Identify the preparation type.
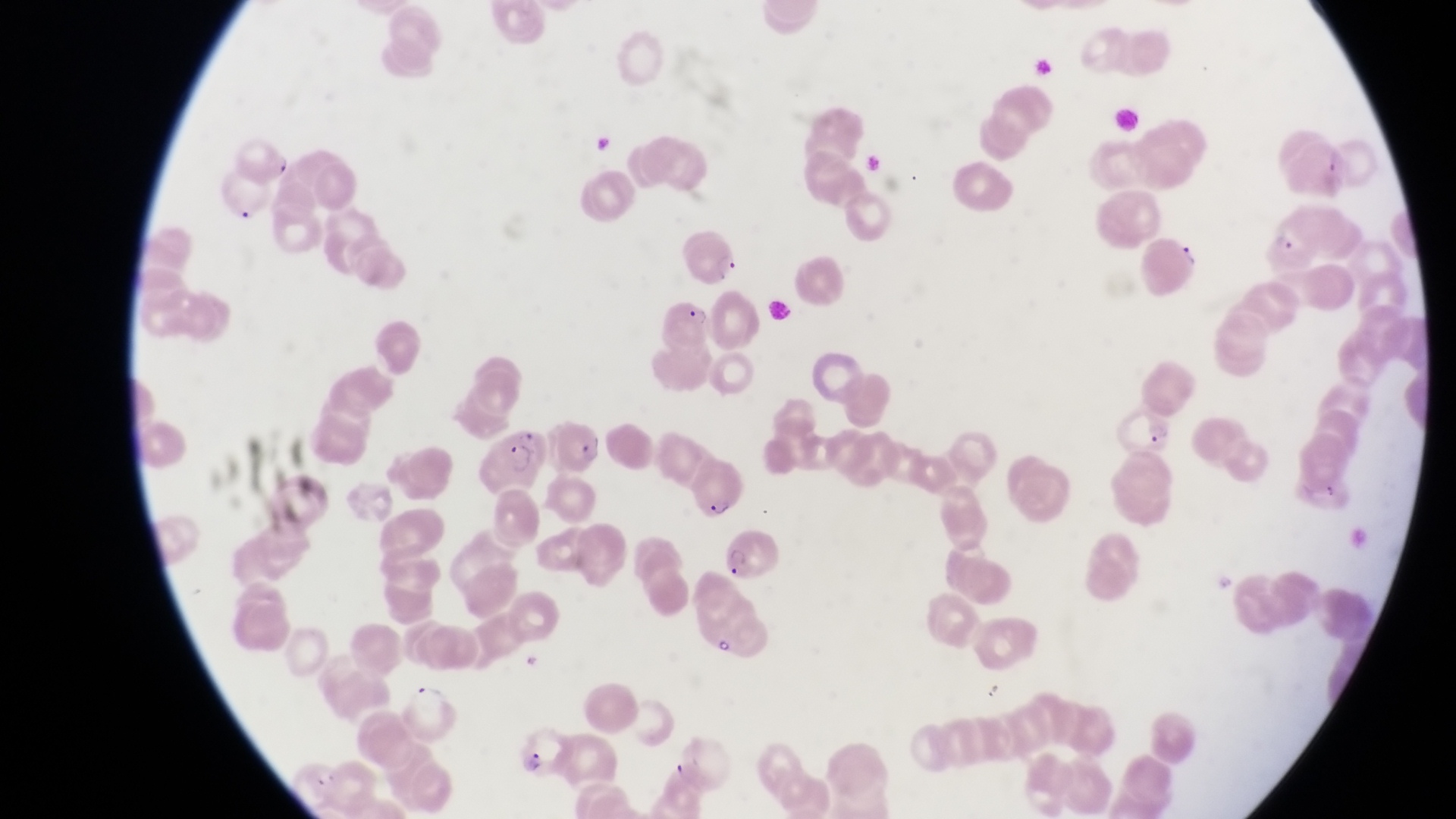
Thin blood smear.

Approximate bounding boxes as [left, top, right, bottom] in pixels.
Summary:
  - Artifact (platelet-like body, stain precipitate, or debris) locations: [716, 629, 737, 659]
  - Trophozoite locations: [713, 249, 743, 282]
  - Parasitised red blood cell locations: [1252, 201, 1318, 273], [1145, 241, 1203, 294], [661, 284, 716, 347], [1110, 403, 1177, 459], [554, 412, 613, 476], [479, 419, 546, 491], [717, 518, 776, 581], [510, 719, 569, 779]
  - Field of view: single
  - Magnification: 1000x
  - Image size: 1456×819 pixels
  - Country: Uganda
  - Capture: smartphone photograph through the eyepiece of an Olympus CX-23 microscope